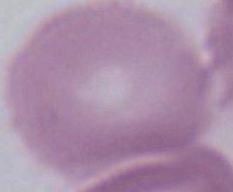
Captured at 1000x magnification. Photomicrograph. A red blood cell is seen.